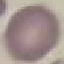
malaria_status: uninfected
preparation: thin blood smear
capture: smartphone camera at the microscope eyepiece
image_type: cell patch, automatically extracted from a larger field of view and resized to 64 × 64 pixels
stain: Giemsa